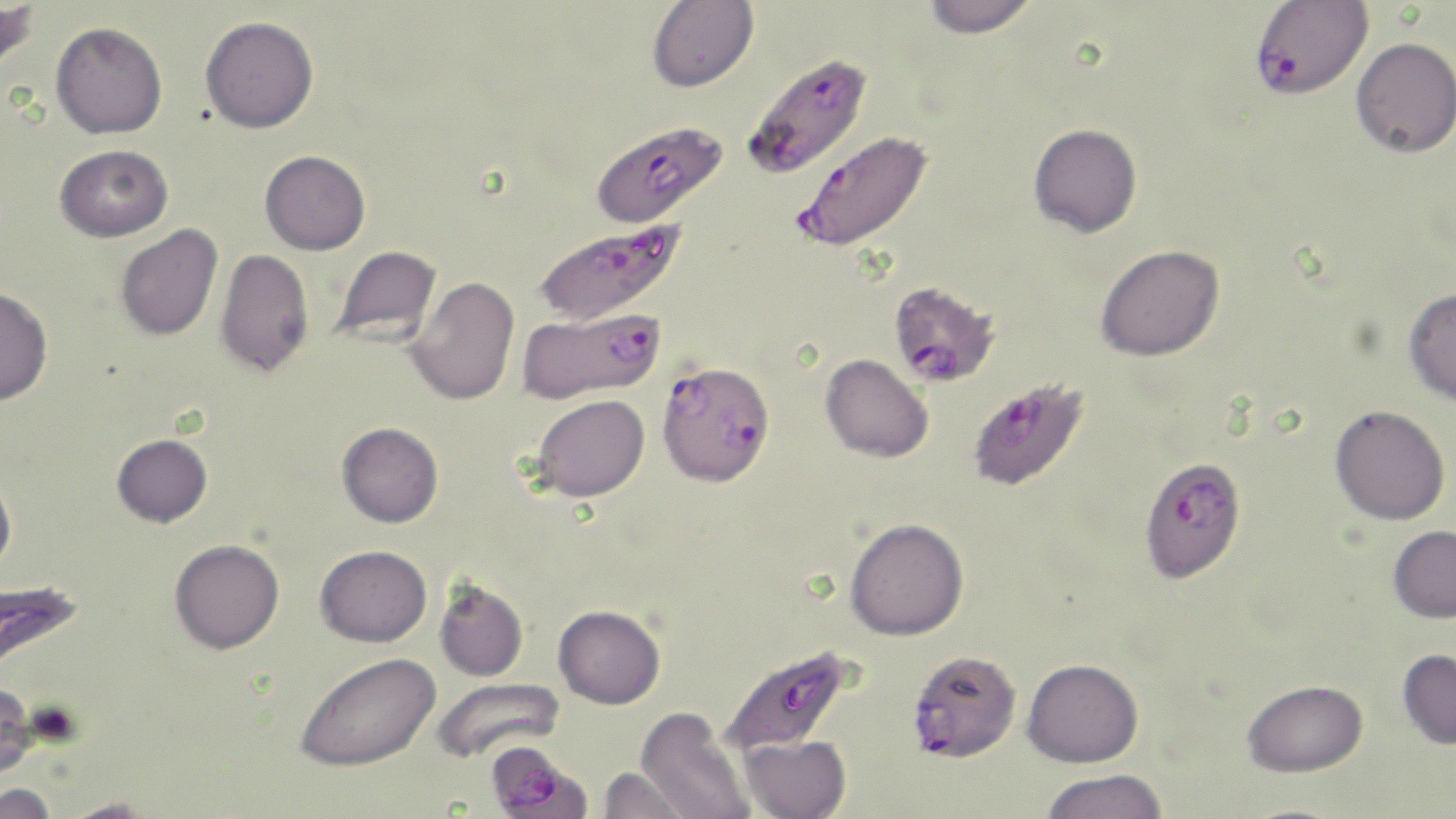

slide_level_diagnosis: Plasmodium falciparum
magnification: 1000x
field_of_view: single
plasmodium_falciparum_infected_red_blood_cell_locations: 'approximate bounding boxes as (x1,y1)-(x2,y2) corner pairs in pixels: (1249,0)-(1373,101), (747,53)-(869,178), (589,119)-(728,230), (791,133)-(933,255), (531,218)-(686,326), (893,294)-(997,389), (517,306)-(667,403), (647,368)-(778,494), (968,371)-(1086,493), (1140,455)-(1235,582), (0,576)-(87,666), (719,645)-(853,759), (908,649)-(1022,763), (485,745)-(589,818)'
preparation: thin blood film
uninfected_red_blood_cell_locations: 'approximate bounding boxes as (x1,y1)-(x2,y2) corner pairs in pixels: (0,0)-(39,77), (647,0)-(759,92), (922,0)-(1037,39), (200,16)-(319,133), (51,21)-(167,138), (1351,36)-(1456,157), (1028,123)-(1142,237), (55,144)-(173,242), (260,150)-(370,254), (115,224)-(222,341), (1095,244)-(1224,361), (331,245)-(442,347), (215,248)-(314,377), (404,276)-(520,406), (0,286)-(53,406), (1403,287)-(1456,406), (821,353)-(934,462), (531,394)-(650,502), (1330,404)-(1450,524), (337,422)-(443,527), (112,433)-(212,527), (0,472)-(17,578), (845,517)-(969,640), (1388,525)-(1456,622), (169,539)-(284,653), (315,544)-(432,647), (434,578)-(529,681), (553,605)-(665,709), (1397,648)-(1456,749), (294,652)-(440,771), (1022,658)-(1144,767), (430,676)-(565,766), (1241,679)-(1369,776), (0,684)-(38,780), (635,707)-(755,819), (738,734)-(852,819), (598,766)-(696,818), (1039,769)-(1167,819), (0,783)-(57,819), (55,798)-(160,818), (1231,802)-(1356,819)'
stain: May-Grünwald-Giemsa
modality: optical microscopy
image_size: 1456×819 pixels